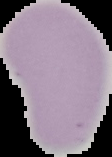
malaria status = uninfected
preparation = thin blood film
image type = segmented cell region on a black background
image size = 112×157 pixels